State which parasite is depicted.
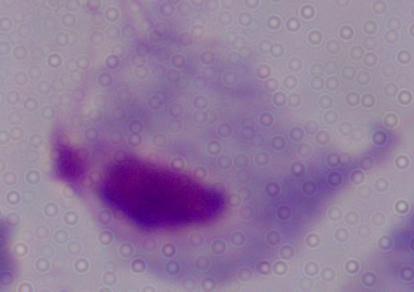

A trichomonad.

Summary:
  - Modality: photomicrograph
  - Magnification: 1000x